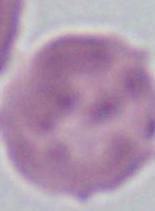
Captured at 1000x magnification. A red blood cell is shown. Micrograph.